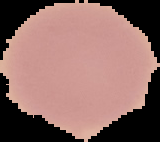

image type = segmented cell region on a black background
malaria status = uninfected
image size = 160×142 pixels
preparation = thin blood film